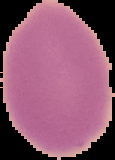

result = no Plasmodium parasites seen
image size = 115×160 pixels
preparation = thin blood film
image type = segmented cell region on a black background